Identify the blood parasite species.
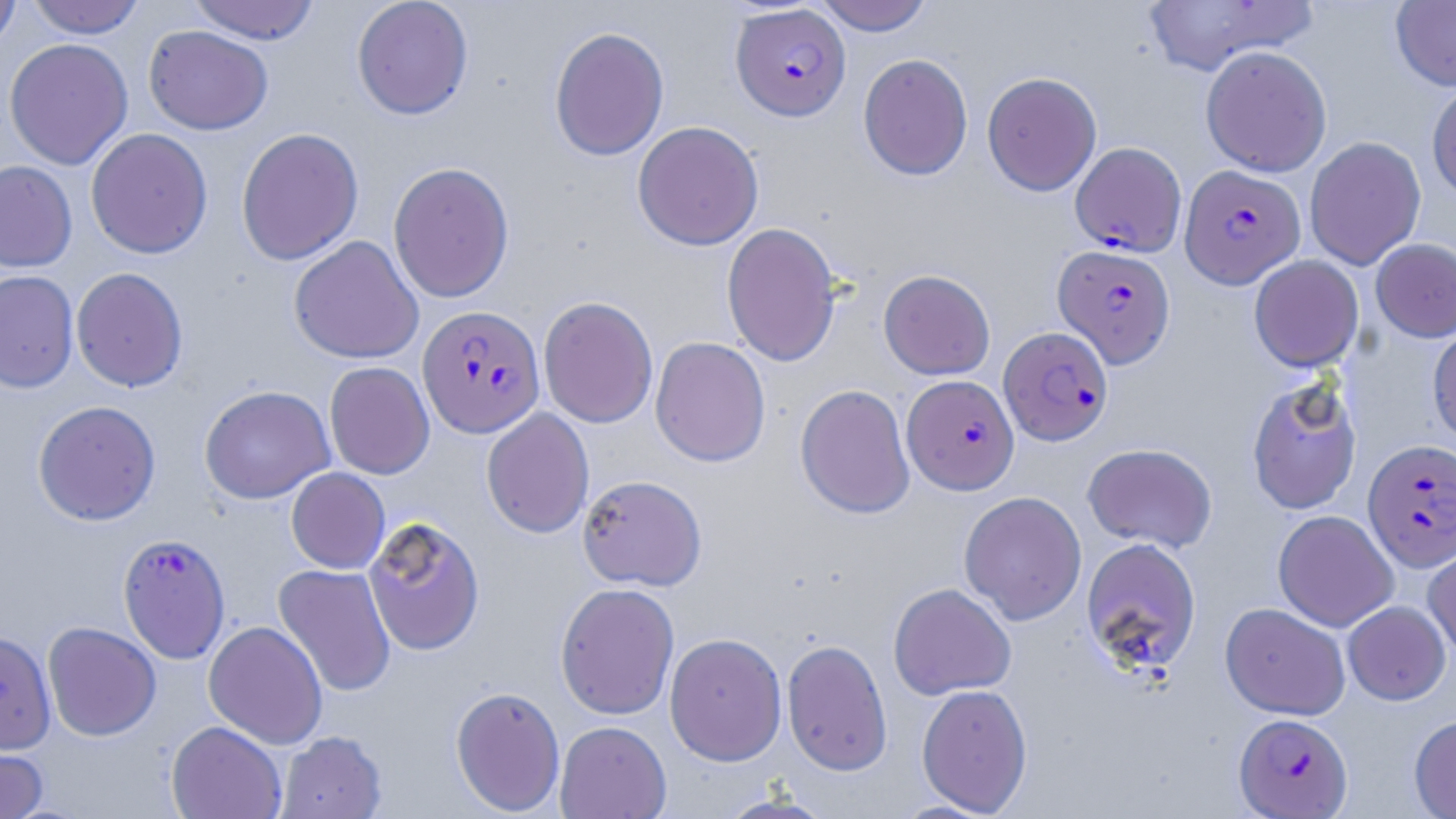
Plasmodium falciparum.

Approximate bounding boxes as [x1, y1, x2, y2] in pixels. Plasmodium falciparum-infected red blood cell locations: [731, 4, 850, 121], [1070, 141, 1187, 256], [1180, 164, 1305, 289], [1053, 244, 1175, 367], [417, 304, 545, 439], [999, 326, 1113, 446], [902, 375, 1019, 495], [1364, 439, 1456, 571], [117, 533, 231, 663], [1234, 713, 1353, 818]. Uninfected red blood cell locations: [0, 0, 21, 53], [27, 0, 146, 39], [188, 0, 321, 44], [352, 0, 473, 120], [813, 0, 934, 35], [1140, 0, 1318, 76], [1390, 0, 1456, 91], [143, 25, 273, 135], [549, 26, 669, 161], [4, 38, 133, 170], [1200, 45, 1332, 177], [858, 53, 973, 180], [981, 71, 1102, 196], [1426, 80, 1456, 202], [632, 120, 763, 250], [236, 127, 364, 266], [86, 128, 213, 259], [1304, 137, 1426, 270], [0, 161, 77, 272], [388, 161, 514, 303], [721, 222, 841, 367], [289, 235, 424, 364], [1370, 238, 1456, 342], [1249, 255, 1364, 372], [70, 267, 188, 392], [879, 269, 995, 380], [0, 270, 79, 393], [538, 296, 658, 428], [1428, 321, 1456, 447], [650, 336, 771, 467], [324, 362, 434, 479], [1245, 378, 1362, 515], [795, 383, 915, 518], [199, 385, 335, 504], [32, 400, 161, 526], [481, 408, 594, 538], [1082, 443, 1217, 553], [286, 467, 390, 574], [577, 474, 707, 591], [959, 491, 1087, 625], [1273, 510, 1398, 632], [363, 516, 485, 656], [1423, 536, 1456, 661], [1080, 537, 1202, 675], [274, 563, 396, 697], [555, 582, 680, 720], [888, 583, 1016, 700], [1342, 601, 1450, 705], [1220, 602, 1350, 720], [203, 620, 328, 749], [42, 621, 161, 741], [0, 630, 56, 753], [664, 632, 787, 765], [781, 639, 893, 775], [916, 683, 1033, 816], [450, 686, 566, 815], [1409, 714, 1456, 818], [166, 721, 287, 819], [554, 721, 671, 819], [276, 730, 388, 819], [0, 737, 49, 819], [716, 791, 836, 819]. Thin blood film. One field of a larger specimen. 1000x magnification. Light microscopy. May-Grünwald-Giemsa stain. Image is 1456×819 pixels.